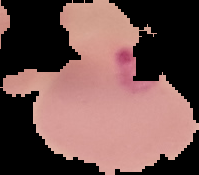

Summary:
  - Malaria status: parasitized
  - Image type: cell region segmented out of the field of view; surrounding area masked to black
  - Preparation: thin blood film
  - Image size: 199×175 pixels